Identify the parasite.
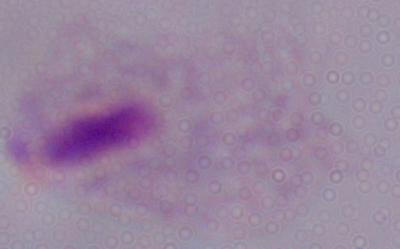
A trichomonad.

Summary:
  - Magnification: 1000x
  - Modality: micrograph